Comment on the morphology of the erythrocytes.
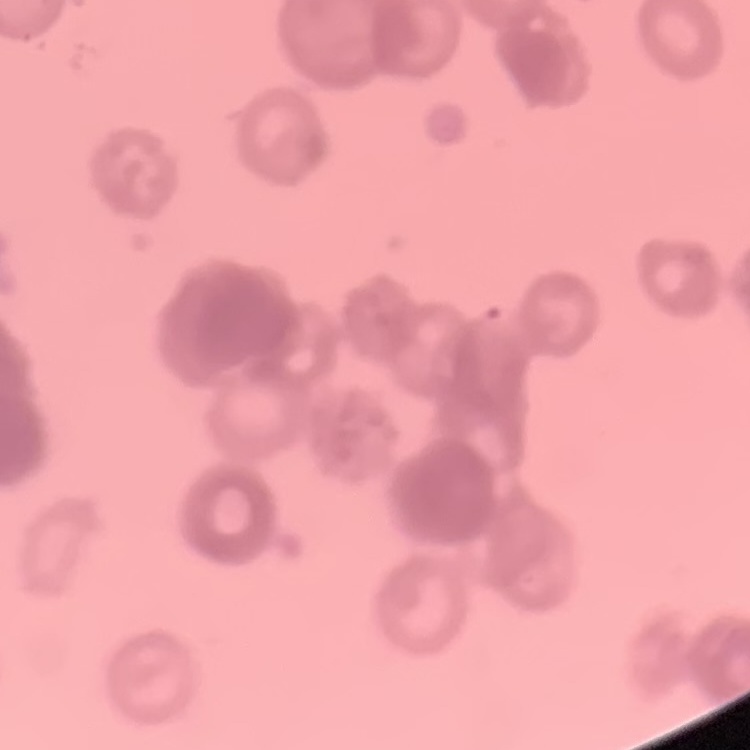

Rouleaux formation.

stain = Field's or Giemsa
image type = one tile cut from a larger photomicrograph
preparation = thin blood film